Identify the parasite.
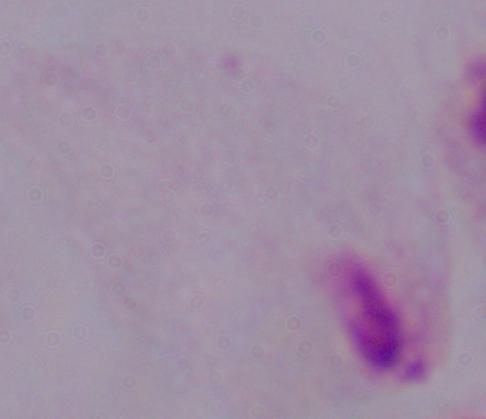

A trichomonad.

Summary:
  - Modality: micrograph
  - Magnification: 1000x